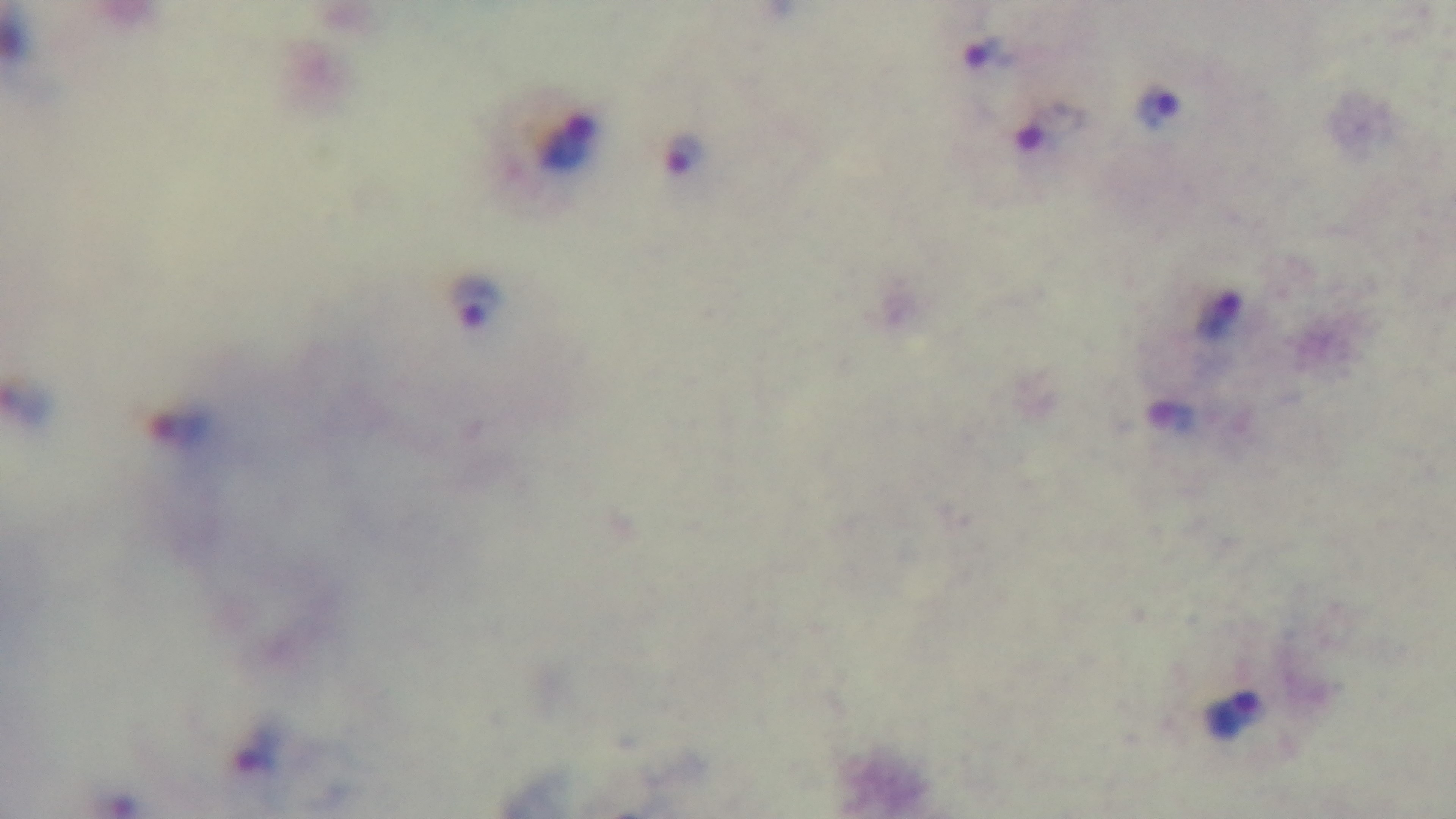 Malaria status: positive. Giemsa-stained. 100x oil-immersion objective. Photomicrograph. Captured with a mounted 4K digital camera. Preparation: thick smear. One field from the slide.